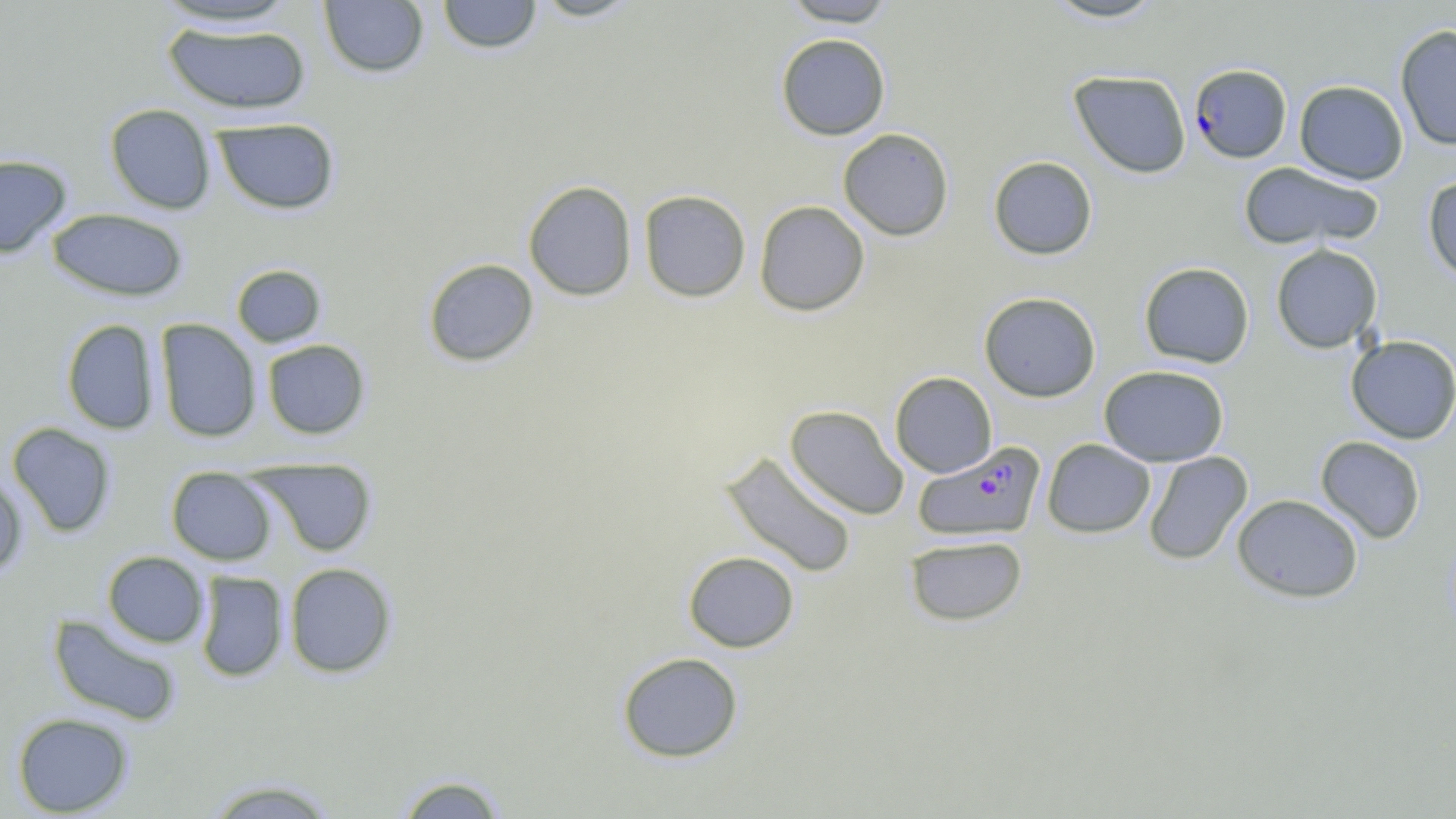 Approximate bounding boxes as (x1, y1, x2, y2) in pixels. Uninfected red blood cell locations: (437, 0, 543, 54), (528, 0, 643, 22), (780, 0, 899, 26), (1042, 0, 1167, 23), (148, 1, 304, 30), (318, 1, 430, 78), (161, 21, 311, 116), (1394, 24, 1456, 150), (775, 34, 891, 140), (1069, 70, 1191, 178), (1294, 80, 1408, 184), (104, 103, 217, 214), (212, 117, 340, 214), (837, 128, 954, 241), (0, 154, 72, 258), (988, 156, 1098, 260), (1238, 162, 1384, 250), (1422, 175, 1456, 283), (523, 180, 637, 301), (638, 189, 751, 302), (754, 200, 870, 316), (46, 208, 189, 301), (1271, 243, 1382, 353), (423, 258, 539, 367), (1139, 262, 1255, 367), (231, 264, 326, 348), (979, 291, 1101, 402), (61, 319, 160, 435), (155, 319, 262, 443), (1346, 335, 1456, 444), (262, 339, 370, 439), (1098, 364, 1229, 466), (890, 371, 997, 477), (784, 405, 909, 520), (7, 422, 117, 537), (1315, 435, 1426, 543), (1042, 438, 1156, 538), (720, 450, 858, 578), (1143, 451, 1253, 565), (249, 457, 377, 557), (166, 466, 277, 565), (0, 472, 27, 579), (1231, 493, 1364, 603), (904, 535, 1027, 626), (102, 551, 209, 648), (683, 551, 800, 652), (284, 562, 397, 678), (195, 571, 289, 682), (48, 613, 182, 726), (616, 651, 744, 763), (12, 712, 134, 816), (391, 772, 511, 818), (201, 777, 342, 819). Plasmodium falciparum-infected red blood cell locations: (1189, 63, 1292, 163), (913, 442, 1046, 541). Slide-level diagnosis: Plasmodium falciparum. May-Grünwald-Giemsa-stained preparation. Optical microscopy. Thin blood film. Captured at 1000x magnification. Single field of view. Image is 1456×819 pixels.